Assess this cell for malaria.
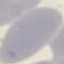
It is uninfected.

Thin blood film. Photographed with a smartphone camera at the microscope eyepiece. Giemsa-stained preparation. Cell patch, automatically extracted from a larger field of view and resized to 64 × 64 pixels.